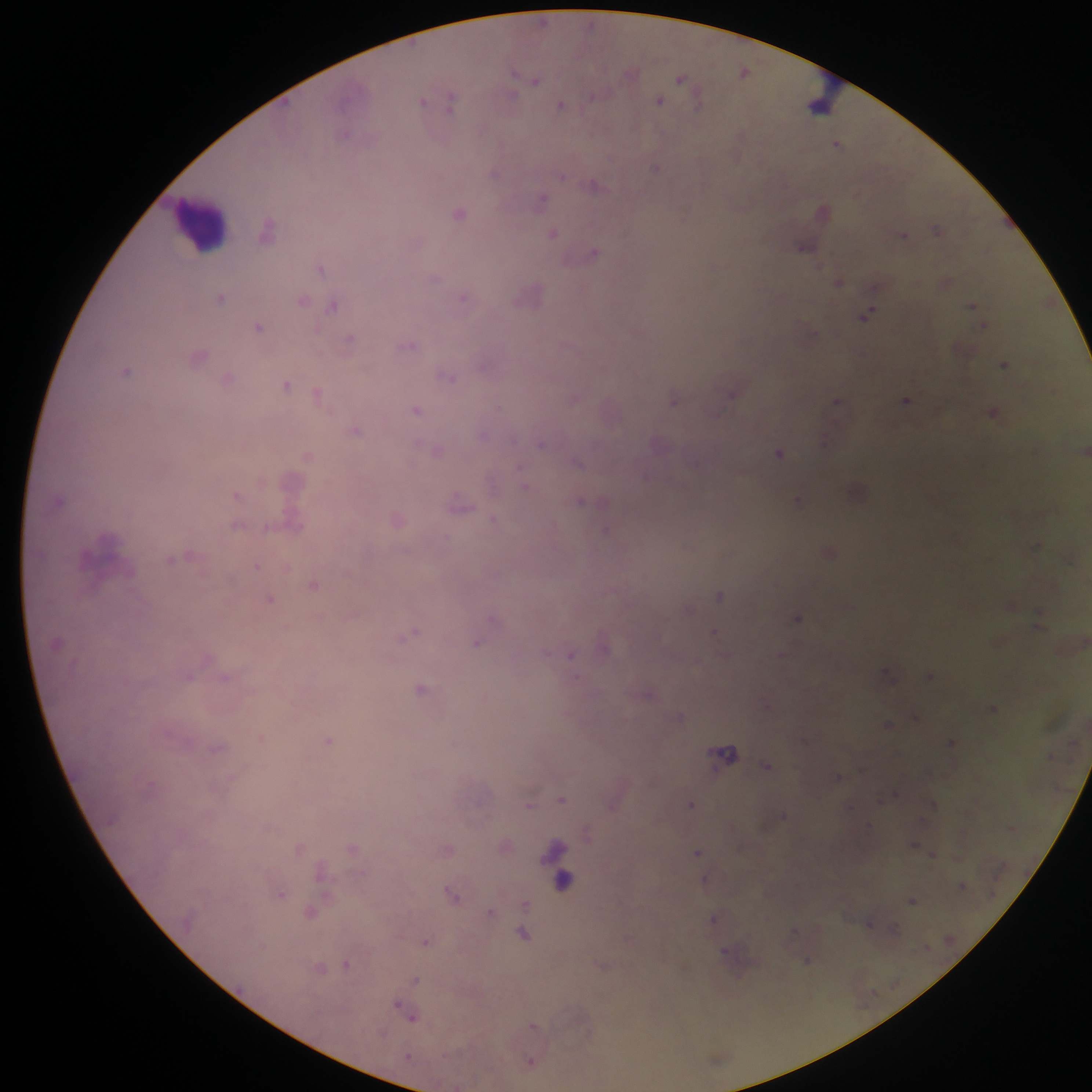
{
  "leukocyte_locations": "approximate centers as {x, y} in pixels: {825, 94}, {200, 222}, {563, 870}",
  "capture": "mobile-phone photograph through a microscope",
  "malaria_parasite_locations": "approximate centers as {x, y} in pixels: {543, 21}, {744, 71}, {513, 72}, {680, 77}, {536, 81}, {512, 97}, {592, 97}, {660, 100}, {423, 101}, {450, 101}, {560, 106}, {345, 133}, {837, 144}, {656, 167}, {494, 172}, {561, 175}, {594, 184}, {542, 201}, {460, 213}, {937, 229}, {268, 230}, {553, 233}, {903, 234}, {804, 245}, {594, 253}, {321, 268}, {436, 278}, {839, 282}, {530, 296}, {221, 297}, {464, 297}, {303, 300}, {333, 305}, {972, 306}, {867, 315}, {983, 325}, {259, 327}, {350, 339}, {408, 345}, {199, 356}, {1005, 364}, {483, 366}, {127, 371}, {448, 376}, {228, 379}, {287, 384}, {731, 392}, {318, 394}, {573, 399}, {906, 399}, {673, 400}, {837, 400}, {499, 407}, {417, 409}, {994, 412}, {356, 429}, {482, 433}, {541, 444}, {437, 450}, {779, 452}, {308, 456}, {578, 462}, {524, 486}, {238, 494}, {59, 500}, {580, 501}, {798, 501}, {459, 504}, {494, 519}, {294, 524}, {238, 525}, {268, 529}, {606, 530}, {175, 558}, {257, 566}, {314, 584}, {720, 596}, {270, 599}, {1011, 604}, {690, 608}, {1037, 616}, {798, 617}, {715, 632}, {411, 633}, {477, 642}, {781, 653}, {571, 654}, {887, 672}, {189, 676}, {929, 676}, {225, 677}, {421, 688}, {649, 694}, {993, 708}, {888, 724}, {328, 740}, {952, 742}, {725, 753}, {766, 765}, {838, 776}, {562, 799}, {690, 804}, {529, 805}, {783, 815}, {914, 844}, {299, 849}, {697, 852}, {933, 854}, {320, 874}, {704, 879}, {961, 885}, {280, 894}, {452, 895}, {912, 900}, {525, 905}, {491, 912}, {311, 913}, {714, 918}, {893, 928}, {792, 932}, {524, 935}, {426, 942}, {726, 954}, {808, 960}, {347, 964}, {415, 978}, {410, 1014}, {409, 1057}, {531, 1061}",
  "country": "Ghana",
  "field_of_view": "single",
  "preparation": "thick blood smear",
  "image_size": "1092×1092 pixels"
}